Describe the morphology of the erythrocytes.
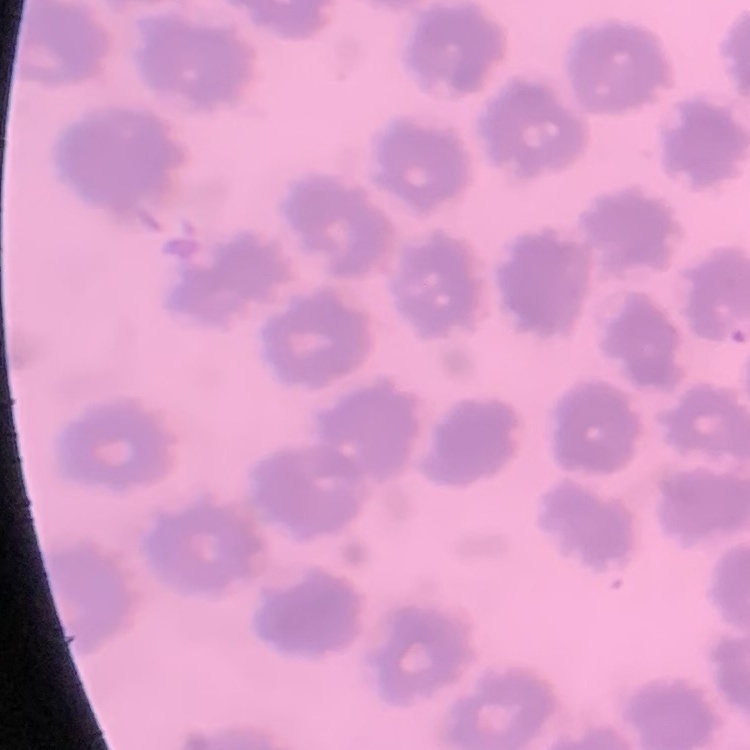
No rouleaux formation.

Thin blood smear. Square crop of a larger photomicrograph. Stained with either Field's or Giemsa.